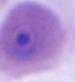
Micrograph. 400x or 1000x magnification. A Plasmodium parasite is seen.